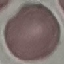

Summary:
  - Malaria status: uninfected
  - Stain: Giemsa
  - Preparation: thin blood smear
  - Capture: smartphone camera at the microscope eyepiece
  - Image type: cell patch, automatically extracted from a larger field of view and resized to 64 × 64 pixels